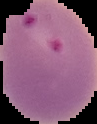

{
  "preparation": "thin blood film",
  "image_type": "segmented cell region with the area outside set to black",
  "malaria_status": "parasitized",
  "image_size": "97×124 pixels"
}